Classify this cell by malaria status.
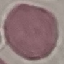

It is uninfected.

Photographed with a smartphone camera at the microscope eyepiece. Giemsa stain. Thin blood film. Cell patch, automatically extracted from a larger field of view and resized to 64 × 64 pixels.